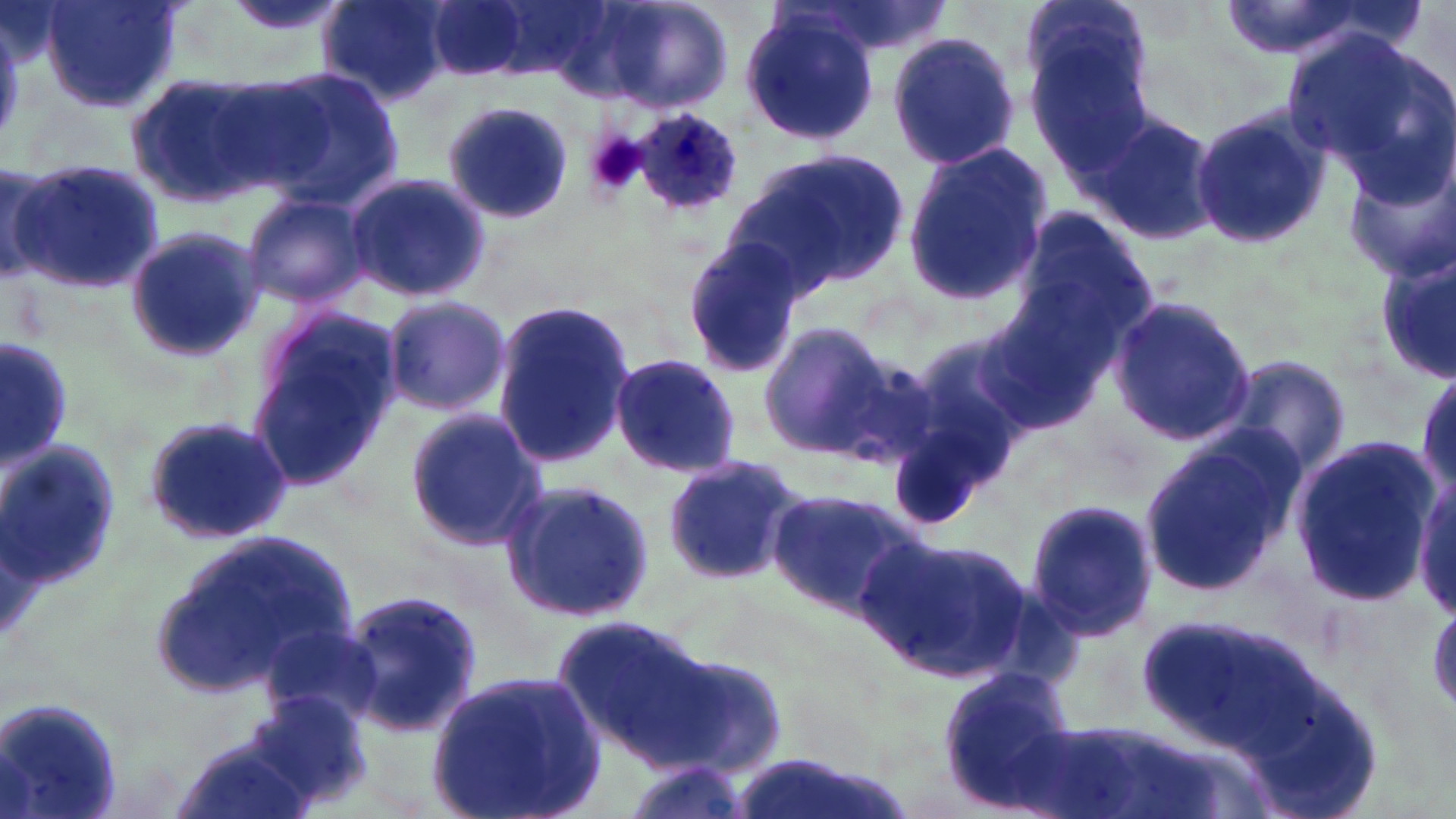
Summary:
  - Coordinate format: approximate bounding boxes as (x1,y1)-(x2,y2) corner pairs in pixels
  - Platelet locations: (586,133)-(647,195)
  - Uninfected red blood cell locations: (38,0)-(185,113), (318,0)-(452,106), (429,0)-(532,78), (1016,0)-(1154,113), (1219,0)-(1411,60), (593,2)-(734,114), (740,10)-(880,145), (1285,26)-(1448,194), (884,29)-(1025,171), (1023,39)-(1157,176), (250,66)-(405,213), (126,71)-(280,209), (444,102)-(575,224), (1083,106)-(1222,246), (1188,108)-(1331,253), (902,141)-(1054,308), (726,150)-(914,295), (1336,154)-(1456,281), (1,162)-(57,285), (10,162)-(164,294), (345,173)-(490,301), (243,193)-(370,309), (1003,204)-(1163,363), (121,224)-(265,362), (681,239)-(807,375), (1380,250)-(1455,385), (379,295)-(512,418), (1108,297)-(1257,445), (491,299)-(634,470), (247,307)-(403,492), (757,323)-(899,461), (1,337)-(73,466), (888,342)-(1028,517), (611,354)-(742,477), (1225,357)-(1351,482), (404,408)-(549,550), (139,410)-(299,544), (1139,432)-(1305,599), (1289,437)-(1438,604), (2,438)-(115,589), (659,456)-(810,589), (1409,472)-(1456,617), (498,480)-(656,622), (766,487)-(926,621), (1024,495)-(1159,645), (148,529)-(364,705), (865,533)-(1029,687), (337,586)-(481,736), (1140,611)-(1323,762), (555,615)-(714,766), (256,617)-(382,730), (650,649)-(791,779), (937,665)-(1079,799), (426,670)-(607,819), (251,690)-(375,805), (1,697)-(125,819), (171,732)-(315,819), (619,758)-(752,819)
  - Plasmodium ovale-infected red blood cell locations: (634,111)-(745,214)
  - Slide-level diagnosis: Plasmodium ovale
  - Field of view: single
  - Preparation: thin blood film
  - Image size: 1456×819 pixels
  - Modality: optical microscopy
  - Magnification: 1000x
  - Stain: May-Grünwald-Giemsa